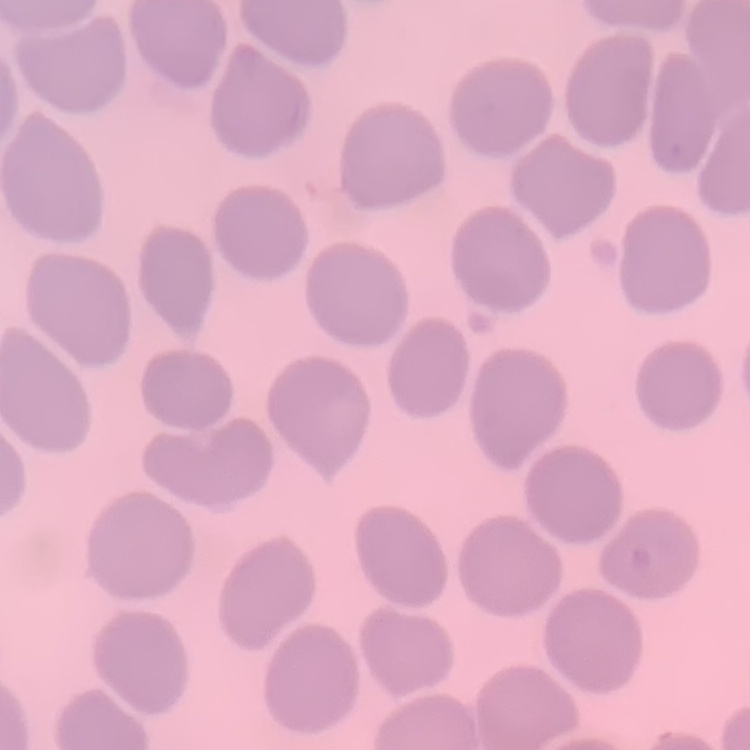 The erythrocytes show no rouleaux formation. Thin blood film. Field's or Giemsa stain. Square crop of a larger photomicrograph.